Name the blood parasite species.
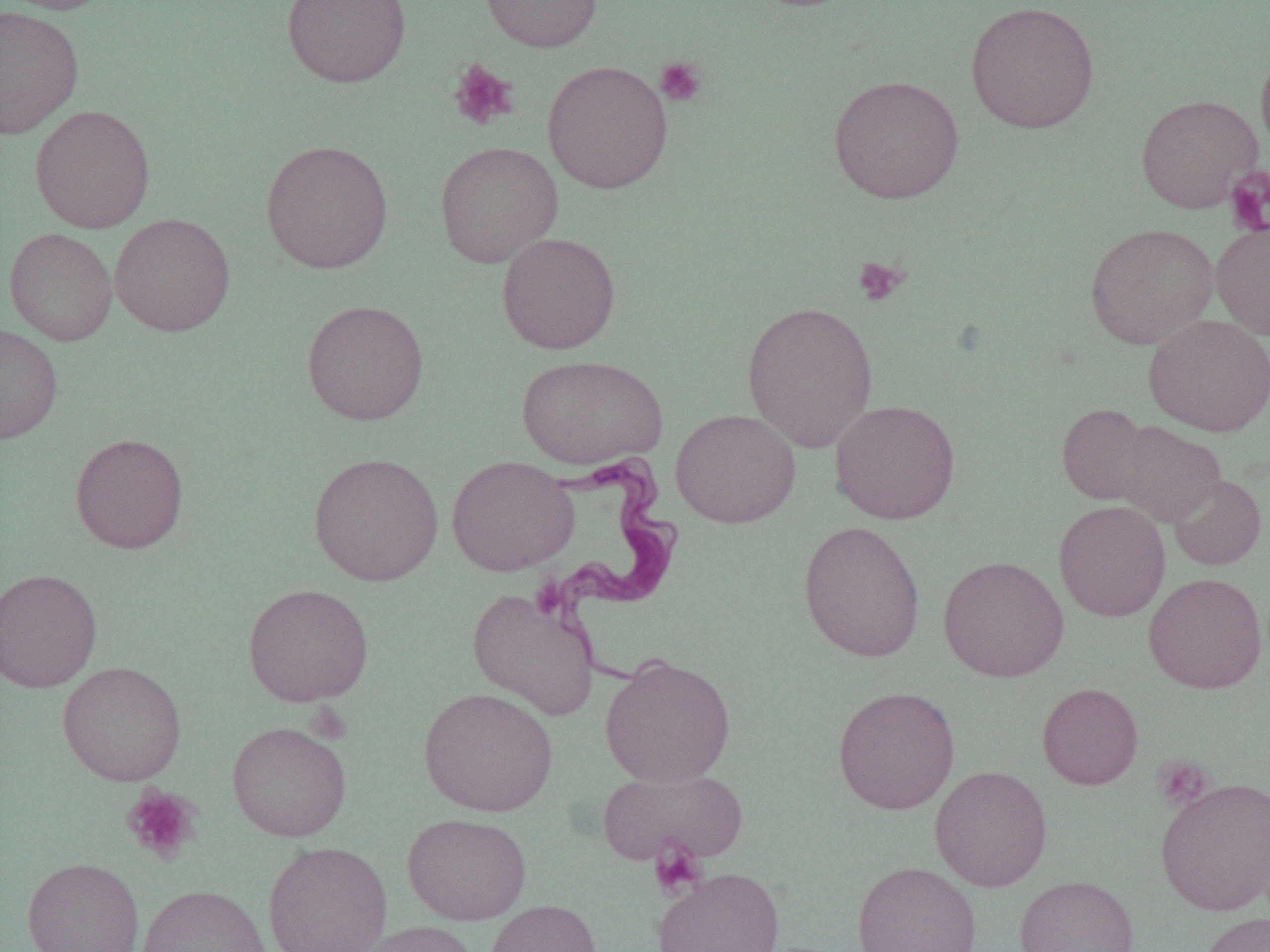
Trypanosoma brucei.

uninfected_red_blood_cell_locations: 'approximate bounding boxes as (x1,y1)-(x2,y2) corner pairs in pixels: (0,0)-(115,15), (281,0)-(411,88), (481,0)-(602,52), (965,1)-(1100,133), (0,5)-(83,138), (1256,48)-(1270,161), (542,60)-(673,194), (828,75)-(964,204), (1136,94)-(1261,212), (30,104)-(155,233), (261,140)-(394,273), (434,141)-(563,267), (109,213)-(235,336), (1210,218)-(1270,340), (1085,223)-(1219,348), (4,228)-(117,345), (497,232)-(620,354), (301,299)-(429,425), (741,302)-(879,452), (1144,314)-(1270,436), (0,322)-(63,445), (516,354)-(668,469), (830,399)-(960,524), (1057,403)-(1153,505), (671,409)-(801,528), (1114,422)-(1225,526), (70,433)-(189,553), (309,452)-(443,587), (446,455)-(579,576), (1168,474)-(1267,569), (1054,500)-(1170,621), (798,520)-(926,663), (938,556)-(1069,682), (0,568)-(102,693), (1144,573)-(1266,693), (242,583)-(374,706), (467,588)-(599,720), (600,655)-(736,787), (57,661)-(187,786), (1037,682)-(1143,790), (832,686)-(960,813), (419,687)-(558,816), (227,721)-(351,842), (930,765)-(1052,892), (597,766)-(747,867), (1156,776)-(1270,915), (401,812)-(532,925), (262,841)-(392,952), (22,857)-(144,952), (852,861)-(982,952), (653,868)-(786,952), (1014,875)-(1139,952), (136,884)-(272,952), (485,899)-(603,952), (1196,911)-(1270,952), (353,920)-(482,952)'
field_of_view: single
magnification: 1000x
modality: optical microscopy
image_size: 1270×952 pixels
trypanosoma_brucei_locations: 'approximate bounding boxes as (x1,y1)-(x2,y2) corner pairs in pixels: (540,450)-(685,689)'
platelet_locations: 'approximate bounding boxes as (x1,y1)-(x2,y2) corner pairs in pixels: (655,56)-(708,107), (448,59)-(519,131), (1226,168)-(1270,236), (854,256)-(908,306), (1152,755)-(1215,811), (122,786)-(201,863), (648,836)-(707,901)'
preparation: thin blood film